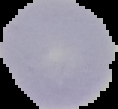
Result: negative for malaria parasites. From a thin blood smear. Segmented cell region on a black background. Image is 118×109 pixels.